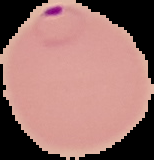

Summary:
  - Malaria status: parasitized
  - Image type: cell region segmented out of the field of view; surrounding area masked to black
  - Image size: 154×160 pixels
  - Preparation: thin blood smear